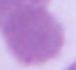 1000x magnification. Photomicrograph. A red blood cell is seen.